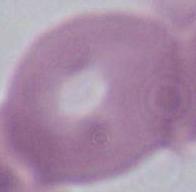 Captured at 1000x magnification. An erythrocyte is shown. Photomicrograph.